Describe the morphology of the erythrocytes.
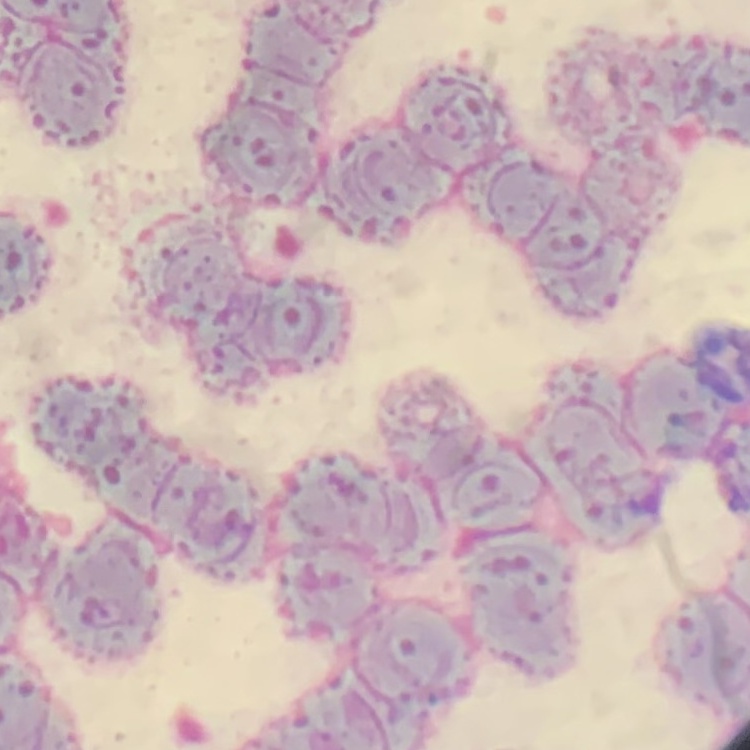
They show rouleaux formation.

Summary:
  - Image type: one tile cut from a larger photomicrograph
  - Stain: Field's or Giemsa
  - Preparation: thin peripheral smear